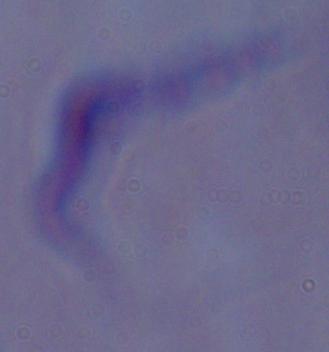

Captured at 1000x magnification. A trypanosome is shown. Photomicrograph.